Report the malaria status of this cell.
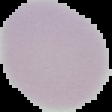

Uninfected.

image type = cell region segmented out of the field of view; surrounding area masked to black
image size = 112×112 pixels
preparation = thin blood film